Classify this cell by malaria status.
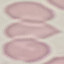

It is uninfected.

capture: smartphone through the microscope eyepiece
image_type: automatically extracted cell patch, resized to 64 × 64 pixels
stain: Giemsa
preparation: thin blood smear